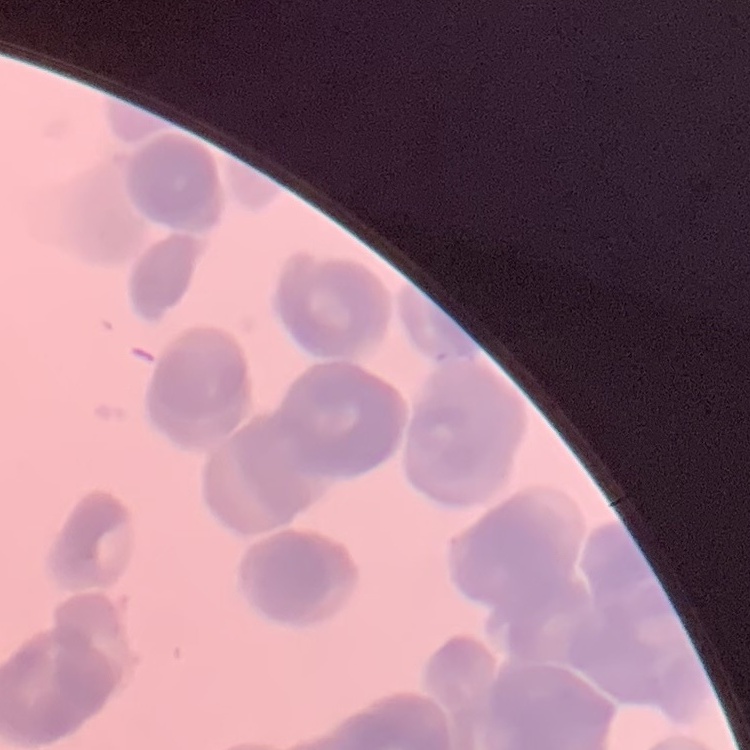

red blood cell morphology = rouleaux formation
image type = square crop of a larger photomicrograph
stain = Field's or Giemsa
preparation = thin blood film